Identify the blood parasite species.
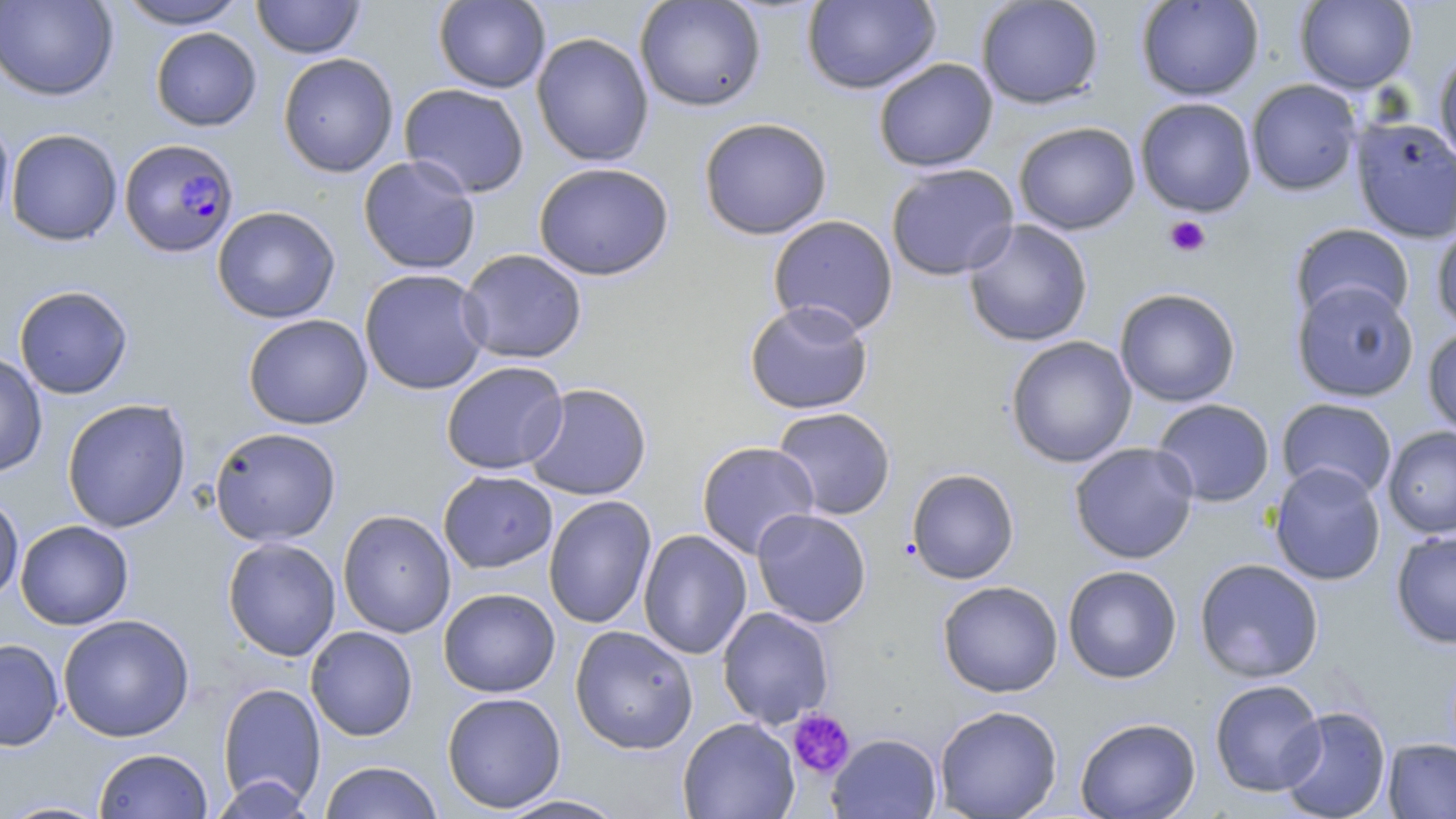

Plasmodium falciparum.

Summary:
  - Coordinate format: approximate bounding boxes as named x1/y1/x2/y2 corners in pixels
  - Uninfected red blood cell locations: (x1=0, y1=0, x2=118, y2=101), (x1=116, y1=0, x2=249, y2=29), (x1=251, y1=0, x2=365, y2=59), (x1=433, y1=0, x2=551, y2=93), (x1=634, y1=0, x2=767, y2=112), (x1=976, y1=0, x2=1104, y2=109), (x1=1136, y1=0, x2=1264, y2=101), (x1=1294, y1=0, x2=1417, y2=93), (x1=802, y1=1, x2=941, y2=95), (x1=150, y1=27, x2=261, y2=131), (x1=531, y1=32, x2=654, y2=167), (x1=1434, y1=50, x2=1456, y2=169), (x1=277, y1=53, x2=399, y2=177), (x1=873, y1=58, x2=998, y2=173), (x1=1246, y1=79, x2=1362, y2=196), (x1=398, y1=83, x2=530, y2=198), (x1=1135, y1=98, x2=1257, y2=217), (x1=0, y1=112, x2=15, y2=235), (x1=1351, y1=116, x2=1456, y2=243), (x1=698, y1=117, x2=832, y2=240), (x1=1013, y1=121, x2=1141, y2=235), (x1=5, y1=128, x2=123, y2=246), (x1=358, y1=155, x2=481, y2=275), (x1=533, y1=161, x2=674, y2=281), (x1=885, y1=163, x2=1020, y2=281), (x1=212, y1=205, x2=341, y2=324), (x1=767, y1=214, x2=899, y2=337), (x1=963, y1=219, x2=1093, y2=347), (x1=1290, y1=223, x2=1414, y2=327), (x1=1431, y1=223, x2=1456, y2=333), (x1=457, y1=248, x2=588, y2=364), (x1=359, y1=268, x2=490, y2=395), (x1=1291, y1=280, x2=1419, y2=402), (x1=14, y1=285, x2=133, y2=399), (x1=1114, y1=288, x2=1240, y2=407), (x1=744, y1=300, x2=874, y2=415), (x1=242, y1=313, x2=373, y2=430), (x1=1422, y1=325, x2=1456, y2=439), (x1=1006, y1=336, x2=1137, y2=468), (x1=0, y1=351, x2=48, y2=478), (x1=441, y1=360, x2=568, y2=475), (x1=523, y1=383, x2=652, y2=501), (x1=1276, y1=397, x2=1398, y2=501), (x1=61, y1=398, x2=191, y2=533), (x1=1152, y1=398, x2=1275, y2=507), (x1=772, y1=407, x2=896, y2=520), (x1=1382, y1=425, x2=1456, y2=539), (x1=209, y1=427, x2=342, y2=546), (x1=696, y1=441, x2=820, y2=559), (x1=1069, y1=442, x2=1199, y2=564), (x1=1268, y1=463, x2=1386, y2=586), (x1=906, y1=468, x2=1019, y2=584), (x1=438, y1=470, x2=558, y2=573), (x1=1, y1=493, x2=24, y2=606), (x1=543, y1=495, x2=657, y2=629), (x1=752, y1=508, x2=872, y2=628), (x1=337, y1=509, x2=456, y2=638), (x1=15, y1=520, x2=134, y2=630), (x1=638, y1=529, x2=752, y2=660), (x1=1391, y1=529, x2=1456, y2=648), (x1=222, y1=537, x2=341, y2=661), (x1=1194, y1=558, x2=1324, y2=683), (x1=1063, y1=565, x2=1182, y2=683), (x1=937, y1=580, x2=1063, y2=697), (x1=438, y1=588, x2=560, y2=698), (x1=717, y1=606, x2=834, y2=728), (x1=57, y1=614, x2=194, y2=742), (x1=570, y1=625, x2=698, y2=754), (x1=305, y1=626, x2=418, y2=741), (x1=0, y1=638, x2=65, y2=751), (x1=1209, y1=679, x2=1326, y2=797), (x1=216, y1=682, x2=326, y2=809), (x1=441, y1=692, x2=566, y2=813), (x1=934, y1=704, x2=1063, y2=818), (x1=1277, y1=705, x2=1391, y2=819), (x1=1075, y1=716, x2=1201, y2=818), (x1=678, y1=717, x2=800, y2=819), (x1=828, y1=733, x2=941, y2=819), (x1=1383, y1=738, x2=1456, y2=818), (x1=93, y1=748, x2=213, y2=819), (x1=318, y1=761, x2=443, y2=819), (x1=210, y1=775, x2=316, y2=818), (x1=495, y1=794, x2=629, y2=818), (x1=3, y1=799, x2=113, y2=818)
  - Plasmodium falciparum-infected red blood cell locations: (x1=119, y1=138, x2=239, y2=257)
  - Platelet locations: (x1=1164, y1=215, x2=1210, y2=258), (x1=787, y1=709, x2=855, y2=780)
  - Stain: May-Grünwald-Giemsa
  - Image size: 1456×819 pixels
  - Magnification: 1000x
  - Modality: optical microscopy
  - Field of view: one of a larger specimen
  - Preparation: thin blood film